Assess the morphology of the erythrocytes.
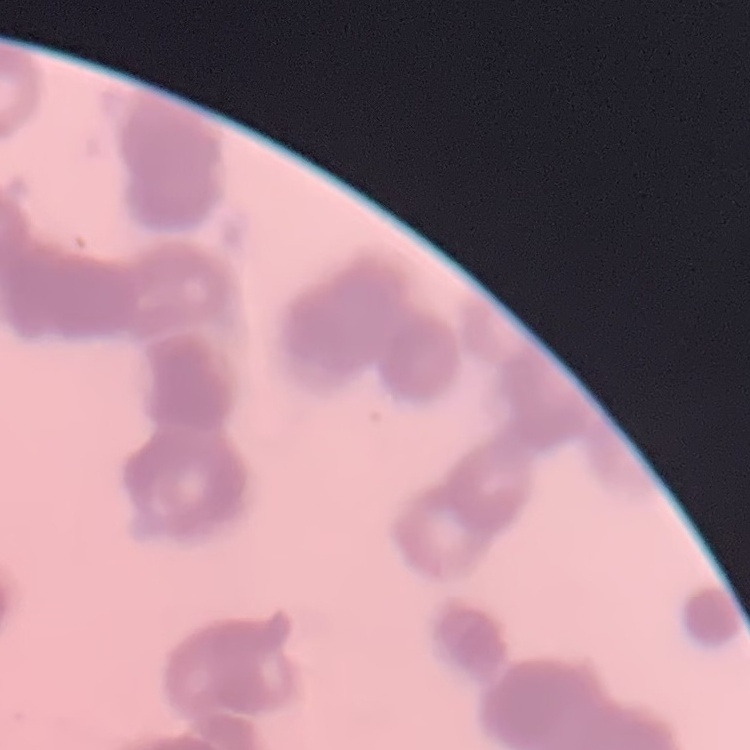

They show rouleaux formation.

Summary:
  - Stain: Field's or Giemsa
  - Preparation: thin peripheral smear
  - Image type: one tile cut from a larger photomicrograph